Assess the morphology of the red blood cells.
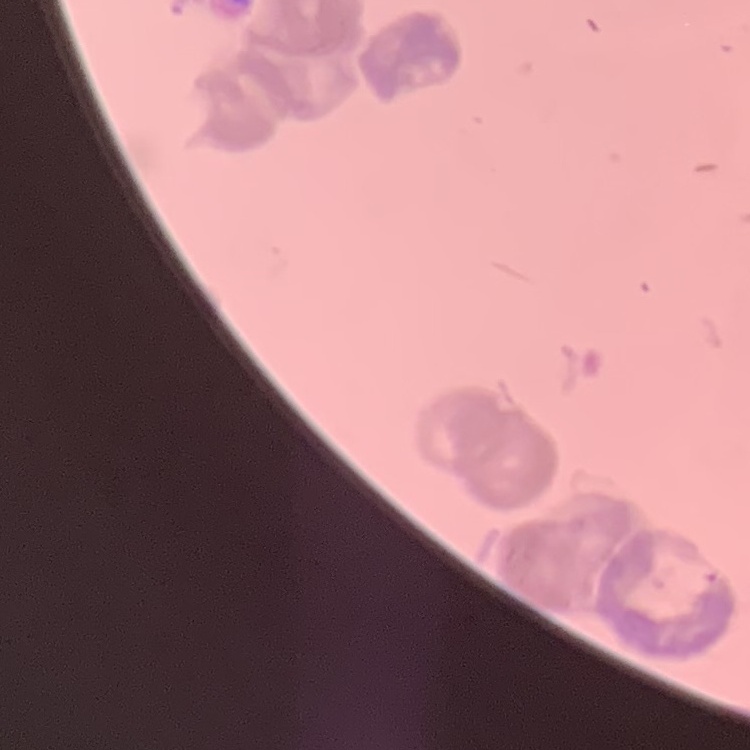
They show rouleaux formation.

Summary:
  - Stain: Field's or Giemsa
  - Preparation: thin blood smear
  - Image type: one tile cut from a larger photomicrograph